Identify the cell.
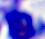

This is a leukocyte.

Photomicrograph. 400x magnification.